Classify this cell by malaria status.
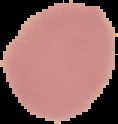
Uninfected.

Summary:
  - Image size: 118×124 pixels
  - Image type: segmented cell region on a black background
  - Preparation: thin blood film